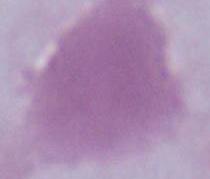
Summary:
  - Identification: red blood cell
  - Magnification: 1000x
  - Modality: micrograph